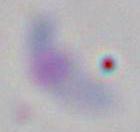
magnification = 1000x
identification = Toxoplasma gondii
modality = photomicrograph